Comment on the morphology of the erythrocytes.
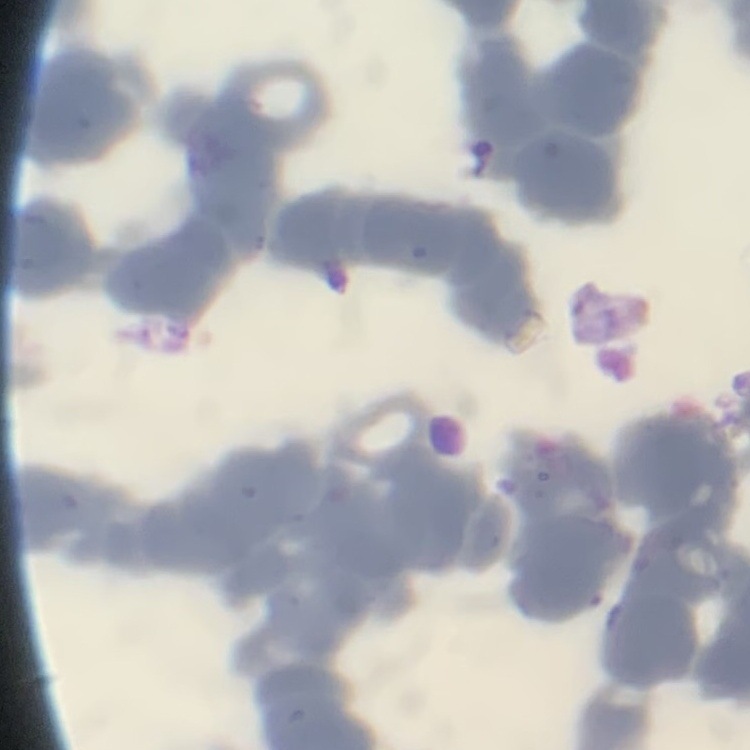

They show rouleaux formation.

preparation = thin peripheral smear
image type = one tile cut from a larger photomicrograph
stain = Field's or Giemsa